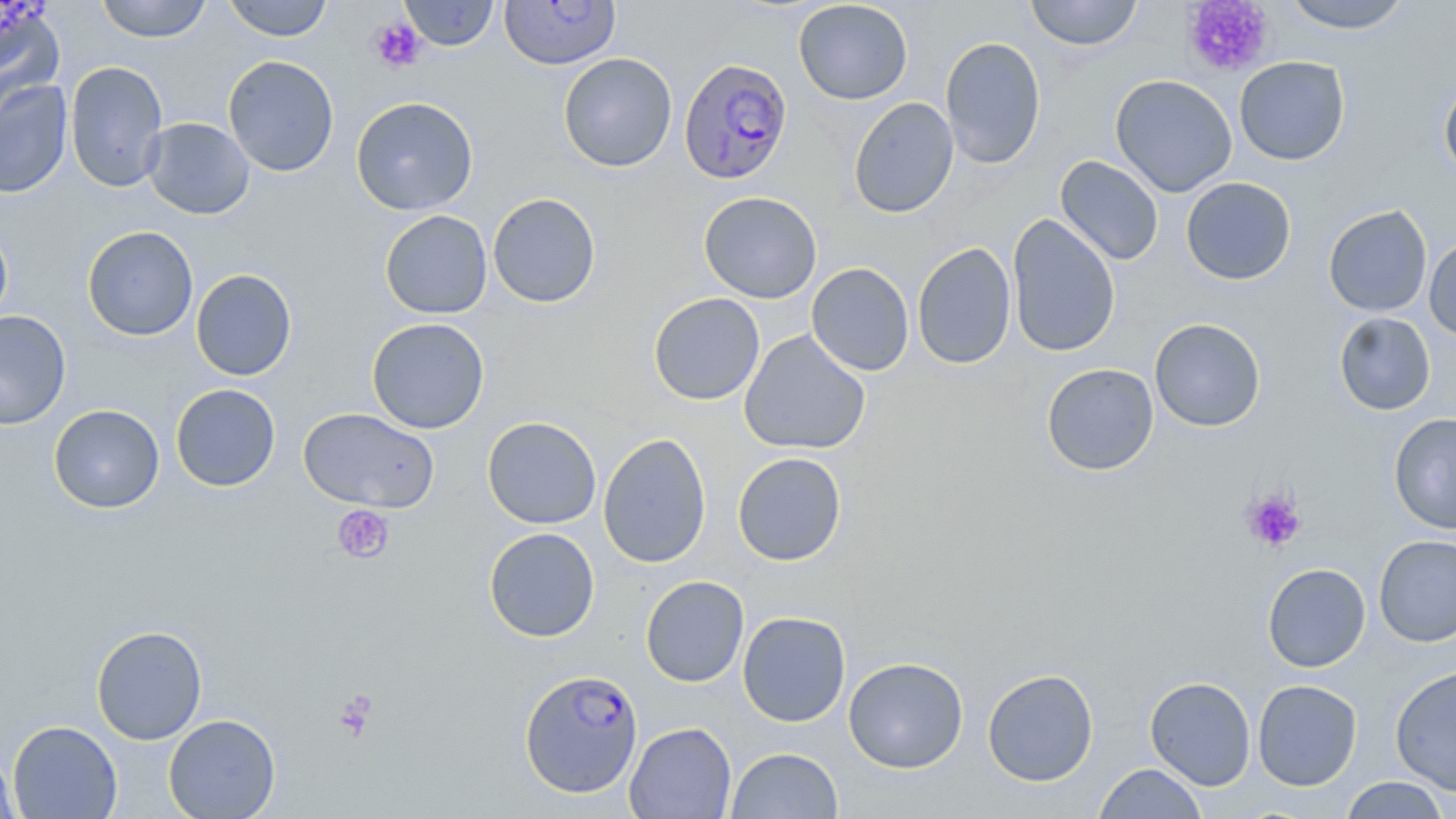
Summary:
  - Coordinate format: approximate bounding boxes as named x1/y1/x2/y2 corners in pixels
  - Plasmodium falciparum-infected red blood cell locations (subset): (x1=678, y1=58, x2=794, y2=185)
  - Platelet locations: (x1=1182, y1=0, x2=1274, y2=78), (x1=368, y1=17, x2=427, y2=73), (x1=1241, y1=489, x2=1306, y2=552), (x1=332, y1=504, x2=394, y2=564), (x1=334, y1=690, x2=378, y2=741)
  - Uninfected red blood cell locations (subset): (x1=0, y1=0, x2=63, y2=99), (x1=95, y1=0, x2=213, y2=43), (x1=221, y1=0, x2=333, y2=41), (x1=398, y1=0, x2=499, y2=51), (x1=499, y1=0, x2=621, y2=70), (x1=1025, y1=0, x2=1143, y2=51), (x1=1279, y1=0, x2=1413, y2=33), (x1=793, y1=1, x2=913, y2=104), (x1=940, y1=36, x2=1046, y2=170), (x1=558, y1=52, x2=677, y2=172), (x1=222, y1=55, x2=339, y2=177), (x1=1234, y1=56, x2=1350, y2=165), (x1=65, y1=60, x2=169, y2=192), (x1=1110, y1=74, x2=1237, y2=197), (x1=1438, y1=77, x2=1456, y2=186), (x1=0, y1=80, x2=73, y2=198), (x1=350, y1=96, x2=478, y2=215), (x1=848, y1=97, x2=959, y2=218), (x1=142, y1=117, x2=255, y2=220), (x1=1055, y1=155, x2=1164, y2=266), (x1=1181, y1=177, x2=1296, y2=285), (x1=698, y1=191, x2=822, y2=304), (x1=488, y1=192, x2=601, y2=308), (x1=1323, y1=205, x2=1432, y2=317), (x1=379, y1=210, x2=493, y2=319), (x1=1007, y1=213, x2=1121, y2=358), (x1=0, y1=220, x2=13, y2=330), (x1=82, y1=225, x2=198, y2=341), (x1=1423, y1=235, x2=1456, y2=339), (x1=912, y1=242, x2=1016, y2=370), (x1=806, y1=262, x2=914, y2=376), (x1=191, y1=269, x2=297, y2=381), (x1=648, y1=293, x2=765, y2=406), (x1=0, y1=310, x2=71, y2=430), (x1=1333, y1=311, x2=1435, y2=415), (x1=366, y1=317, x2=489, y2=434), (x1=1149, y1=318, x2=1266, y2=432), (x1=739, y1=330, x2=871, y2=455), (x1=1041, y1=362, x2=1158, y2=476), (x1=170, y1=384, x2=281, y2=491), (x1=49, y1=404, x2=165, y2=513), (x1=298, y1=407, x2=439, y2=512), (x1=1388, y1=413, x2=1456, y2=535), (x1=482, y1=416, x2=602, y2=529), (x1=598, y1=433, x2=712, y2=568), (x1=732, y1=452, x2=847, y2=565), (x1=484, y1=527, x2=600, y2=642), (x1=1374, y1=535, x2=1456, y2=647), (x1=1262, y1=563, x2=1371, y2=672), (x1=640, y1=575, x2=750, y2=688), (x1=737, y1=611, x2=851, y2=727), (x1=91, y1=625, x2=207, y2=745), (x1=843, y1=657, x2=968, y2=773), (x1=1390, y1=665, x2=1456, y2=795), (x1=982, y1=668, x2=1099, y2=786), (x1=1145, y1=676, x2=1256, y2=790), (x1=1252, y1=679, x2=1362, y2=791), (x1=163, y1=714, x2=281, y2=819), (x1=8, y1=720, x2=122, y2=818), (x1=624, y1=722, x2=737, y2=818), (x1=1, y1=744, x2=20, y2=819), (x1=726, y1=747, x2=844, y2=818), (x1=1093, y1=762, x2=1208, y2=818), (x1=1339, y1=776, x2=1452, y2=818)
  - Slide-level diagnosis: Plasmodium falciparum
  - Magnification: 1000x
  - Preparation: thin blood smear
  - Field of view: one of a larger specimen
  - Image size: 1456×819 pixels
  - Modality: light microscopy
  - Stain: May-Grünwald-Giemsa